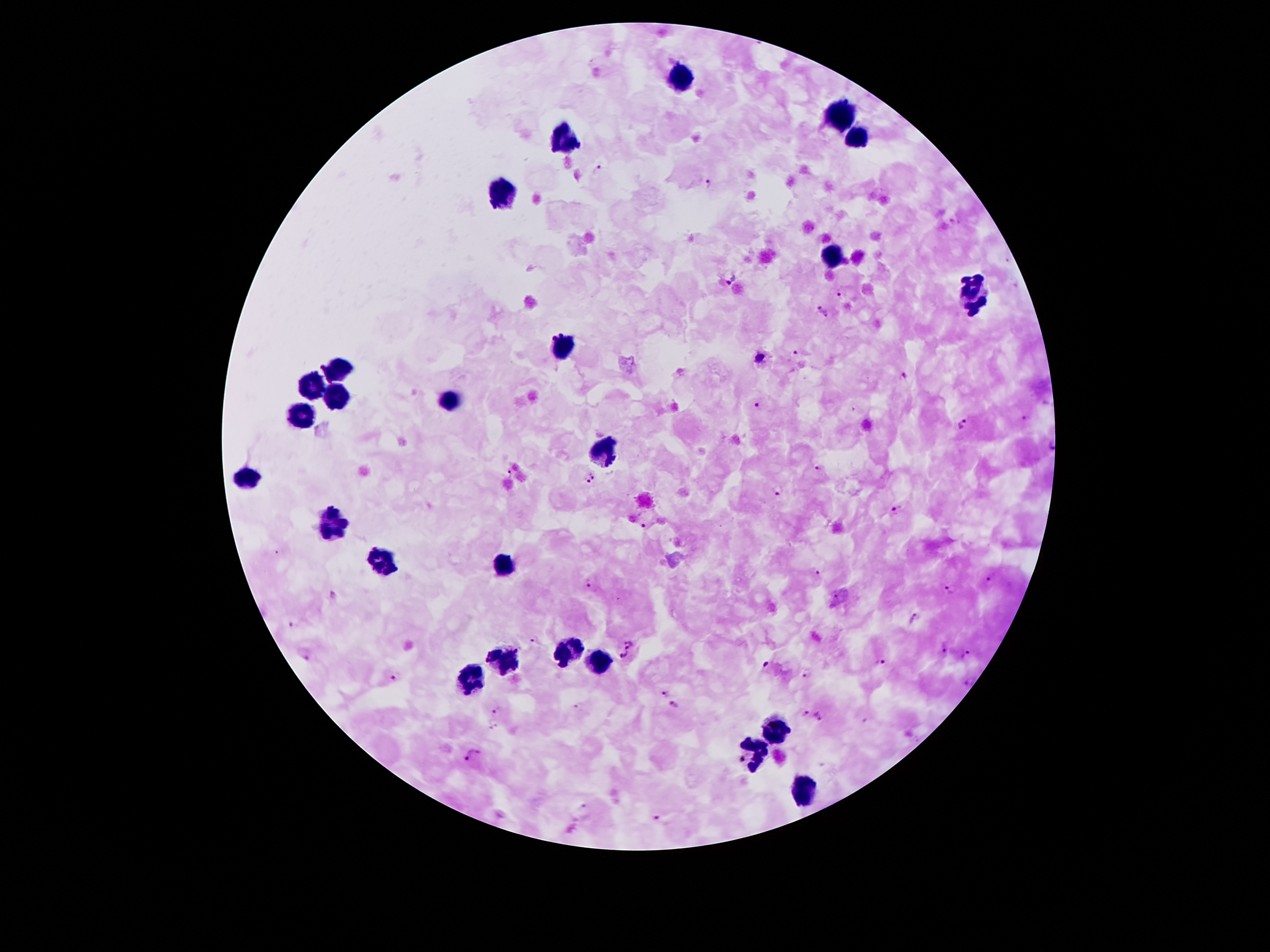

Approximate centers as [x, y] in pixels.
Summary:
  - Leukocyte locations: [681, 78], [843, 118], [856, 139], [564, 143], [503, 194], [835, 256], [970, 288], [973, 307], [563, 345], [335, 370], [311, 390], [339, 398], [447, 401], [303, 416], [609, 454], [247, 477], [332, 523], [385, 564], [503, 566], [571, 651], [502, 661], [599, 661], [472, 676], [775, 730], [755, 753], [802, 791]
  - Malaria parasite locations: [599, 170], [708, 182], [730, 277], [840, 292], [823, 312], [797, 353], [760, 358], [903, 375], [757, 407], [1028, 419], [964, 423], [1050, 445], [819, 470], [508, 473], [590, 478], [777, 491], [897, 510], [643, 525], [816, 571], [990, 582], [590, 583], [950, 590], [332, 594], [915, 618], [291, 625], [535, 639], [629, 644], [944, 648], [966, 654], [624, 655], [306, 656], [881, 662], [766, 663], [808, 673], [392, 677], [968, 681], [664, 693], [674, 704], [577, 706], [497, 712], [804, 712], [820, 716], [493, 724], [476, 751], [466, 762], [584, 806], [657, 819]
  - Magnification: 100x
  - Image size: 1270×952 pixels
  - Field of view: one from this slide
  - Patient malaria status: infected with Plasmodium falciparum
  - Stain: Giemsa
  - Capture: smartphone camera through the microscope eyepiece
  - Preparation: thick blood film